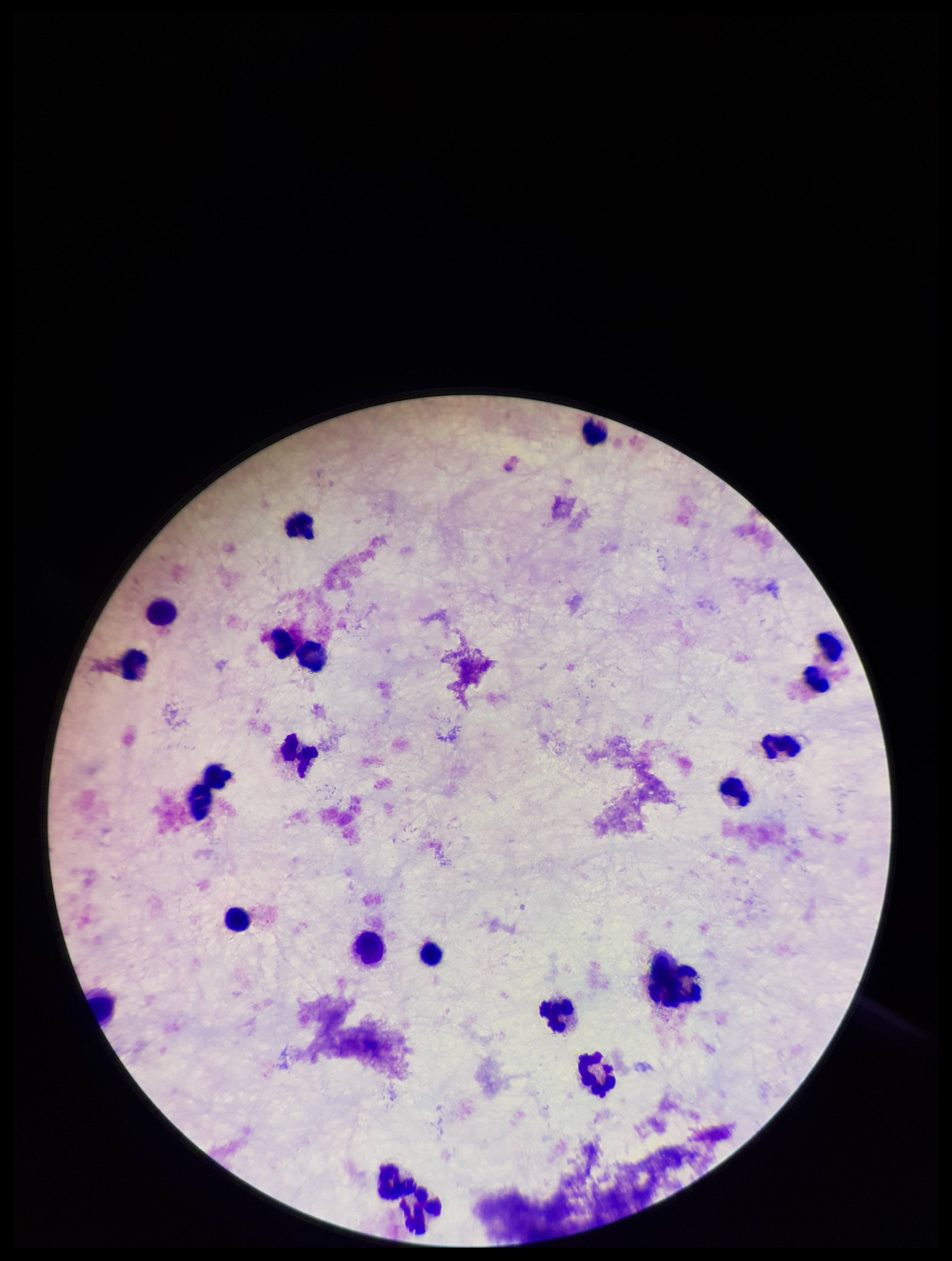

Summary:
  - Preparation: thick
  - Field of view: one from this slide
  - Stain: Giemsa
  - Parasite count: 0
  - Patient malaria status: negative
  - Image size: 952×1261 pixels
  - Capture: smartphone photograph through the microscope eyepiece
  - Leukocyte count: 22
  - Plasmodium parasites: none seen